Name the parasite shown.
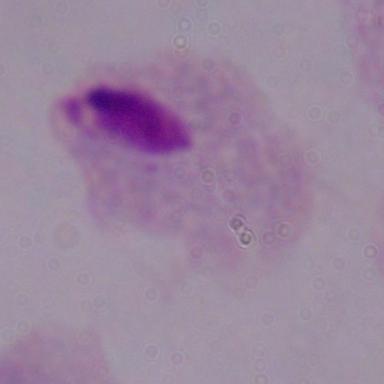

A trichomonad.

Summary:
  - Magnification: 1000x
  - Modality: micrograph